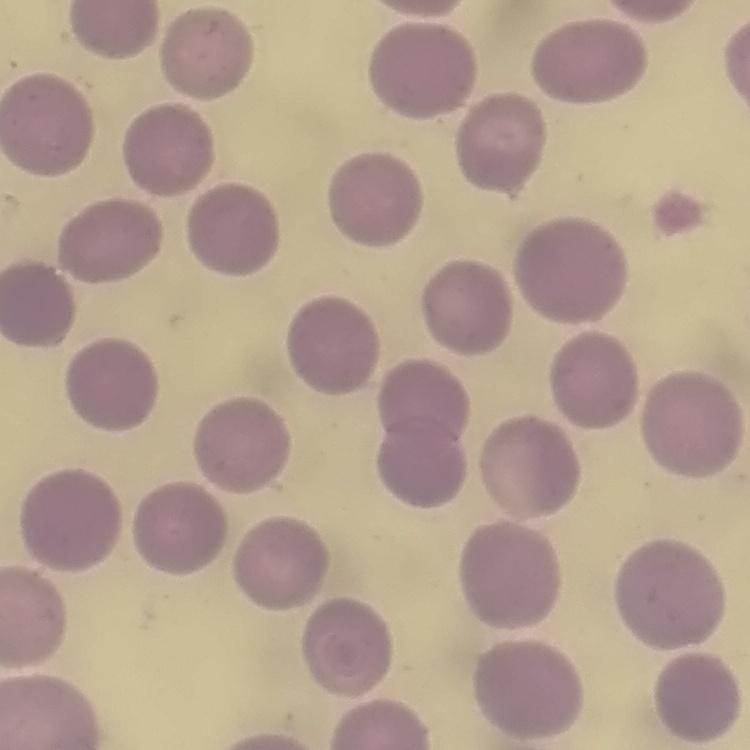
Summary:
  - Red blood cell morphology: no rouleaux formation
  - Stain: Field's or Giemsa
  - Image type: one tile cut from a larger photomicrograph
  - Preparation: thin blood smear